Classify this cell by malaria status.
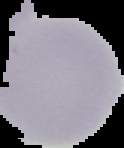

It is uninfected.

Image is 124×148 pixels. From a thin blood film. Segmented cell region on a black background.